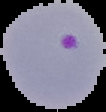 Image is 106×112 pixels. From a thin blood smear. Malaria status: parasitized. The area outside the segmented cell region is set to black.